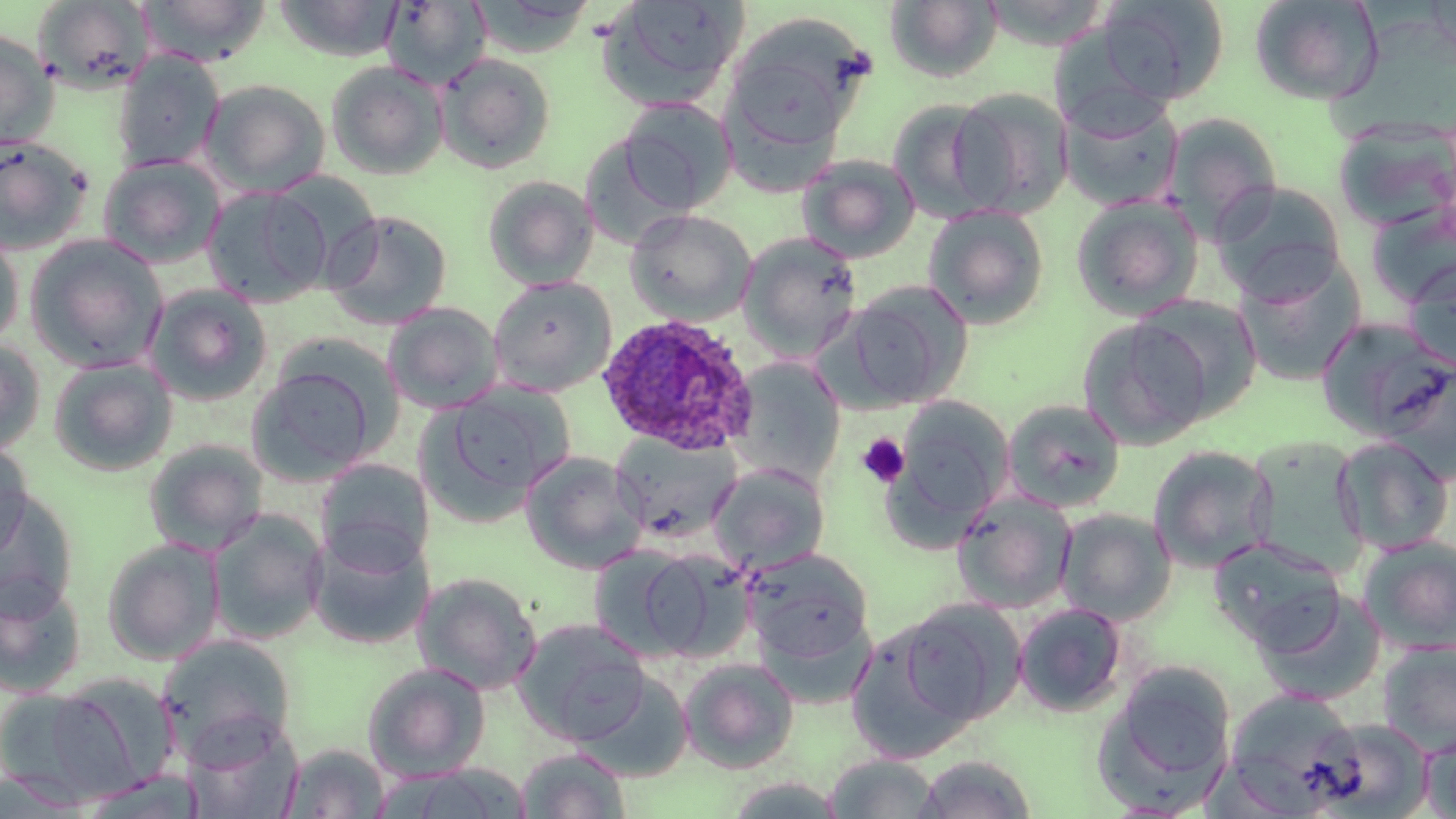

Approximate bounding boxes as (x1, y1, x2, y2) in pixels. Platelet locations: (856, 433, 910, 488). Uninfected red blood cell locations: (138, 0, 271, 66), (274, 0, 404, 61), (381, 0, 491, 89), (597, 0, 748, 110), (886, 0, 1003, 83), (1097, 0, 1229, 106), (1249, 0, 1383, 105), (34, 1, 155, 93), (726, 16, 870, 149), (0, 29, 57, 149), (111, 51, 225, 172), (435, 52, 556, 174), (325, 61, 448, 180), (201, 79, 332, 197), (948, 87, 1073, 218), (1060, 96, 1184, 211), (618, 98, 738, 214), (887, 100, 1005, 223), (1161, 113, 1283, 239), (1334, 121, 1456, 231), (0, 136, 92, 255), (99, 154, 225, 268), (797, 154, 920, 263), (481, 175, 600, 290), (1209, 182, 1347, 303), (202, 186, 331, 307), (1071, 194, 1204, 321), (1366, 199, 1456, 311), (922, 205, 1051, 330), (322, 209, 453, 330), (624, 209, 757, 325), (0, 227, 24, 350), (737, 231, 863, 360), (24, 234, 169, 372), (1234, 255, 1367, 388), (1403, 256, 1456, 374), (488, 276, 617, 396), (838, 280, 973, 410), (144, 284, 273, 406), (1130, 293, 1264, 421), (382, 302, 504, 414), (1077, 318, 1213, 450), (1316, 318, 1453, 441), (0, 339, 46, 456), (48, 357, 178, 476), (728, 357, 847, 487), (1379, 358, 1456, 482), (248, 367, 378, 484), (424, 383, 574, 514), (892, 395, 1014, 530), (1002, 399, 1127, 513), (610, 431, 742, 545), (1240, 436, 1371, 577), (1333, 436, 1454, 555), (0, 439, 34, 561), (143, 439, 268, 556), (1148, 445, 1278, 573), (520, 452, 648, 574), (314, 458, 434, 572), (709, 463, 831, 575), (0, 488, 79, 619), (951, 491, 1078, 613), (1056, 508, 1176, 625), (208, 509, 329, 644), (307, 527, 434, 650), (1357, 534, 1456, 655), (1209, 536, 1346, 652), (101, 538, 224, 664), (586, 545, 715, 662), (743, 548, 873, 665), (413, 572, 543, 695), (0, 574, 87, 698), (1254, 587, 1387, 707), (898, 599, 1027, 725), (1013, 602, 1129, 718), (512, 618, 650, 746), (846, 622, 979, 762), (159, 635, 296, 759), (1377, 640, 1456, 757), (678, 657, 800, 774), (362, 662, 491, 782), (1093, 664, 1237, 813), (576, 669, 695, 783), (48, 675, 179, 798), (0, 688, 127, 807), (1223, 690, 1362, 813), (1306, 717, 1433, 818), (185, 718, 304, 818), (1421, 732, 1456, 818), (281, 744, 390, 818), (517, 747, 630, 818), (824, 754, 940, 817), (915, 755, 1036, 818), (393, 765, 531, 818), (0, 771, 89, 817), (74, 771, 203, 818), (721, 777, 849, 818). Plasmodium ovale-infected red blood cell locations: (594, 313, 758, 454). Slide-level diagnosis: Plasmodium ovale. Thin blood smear. Single field of view. May-Grünwald-Giemsa stain. Captured at 1000x magnification. Image is 1456×819 pixels. Light microscopy.